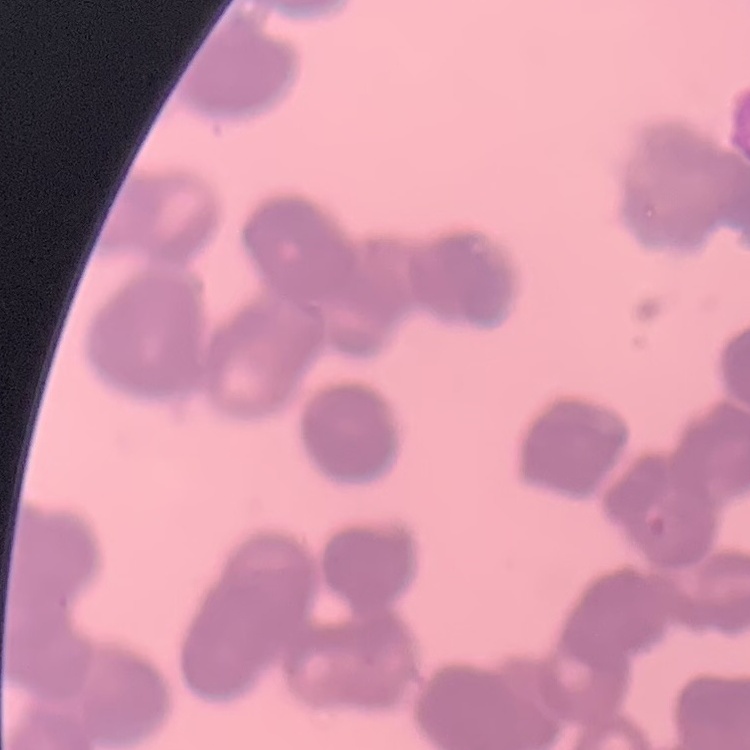
Summary:
  - Red blood cell morphology: rouleaux formation
  - Image type: square crop of a larger photomicrograph
  - Stain: Field's or Giemsa
  - Preparation: thin blood smear